Locate every blood parasite and identify its species.
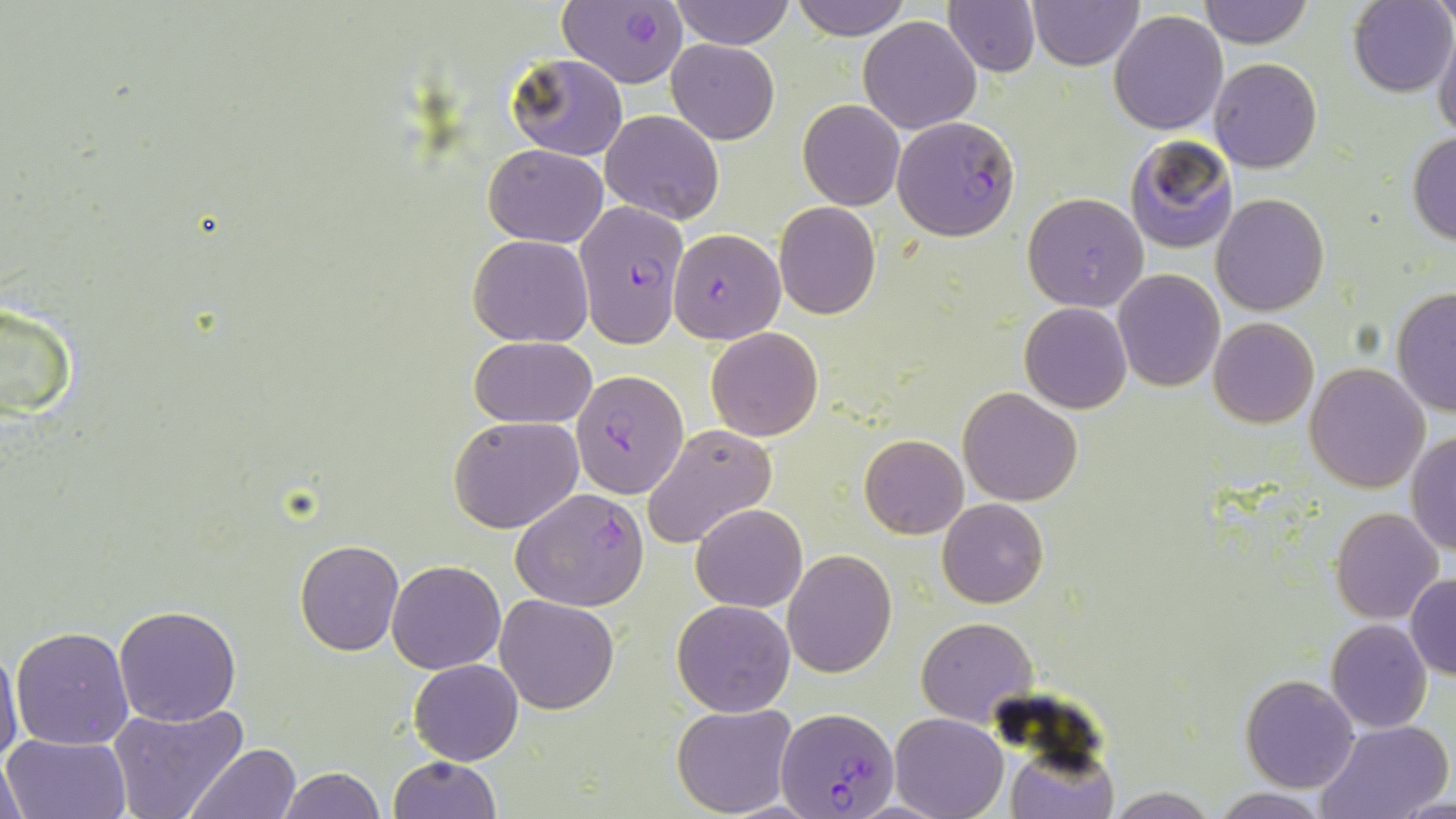

Approximate bounding boxes as (x1, y1, x2, y2) in pixels.
Plasmodium falciparum-infected red blood cells: (555, 1, 688, 89), (891, 116, 1020, 240), (573, 199, 690, 346), (668, 228, 785, 344), (572, 368, 690, 498), (511, 488, 649, 611), (777, 707, 898, 818).
No Plasmodium ovale, Plasmodium malariae, Plasmodium vivax, Babesia divergens, or Trypanosoma brucei observed.

Summary:
  - Uninfected red blood cell locations: (669, 0, 793, 49), (789, 0, 911, 40), (1199, 0, 1311, 47), (944, 1, 1040, 76), (1029, 1, 1141, 70), (1347, 1, 1454, 97), (1110, 9, 1227, 134), (1389, 12, 1452, 124), (859, 16, 981, 134), (1432, 25, 1456, 143), (666, 38, 779, 144), (505, 52, 627, 161), (1209, 57, 1322, 173), (798, 99, 904, 210), (601, 110, 725, 226), (1407, 132, 1456, 245), (1124, 135, 1238, 253), (484, 142, 608, 247), (1023, 192, 1149, 313), (1211, 193, 1329, 315), (774, 202, 881, 320), (468, 234, 593, 346), (1113, 269, 1225, 392), (1390, 285, 1456, 418), (1, 302, 78, 418), (1020, 302, 1131, 413), (1208, 317, 1318, 428), (706, 327, 823, 442), (470, 336, 597, 429), (1305, 364, 1431, 493), (958, 386, 1084, 505), (449, 417, 585, 534), (642, 424, 778, 548), (1407, 431, 1456, 556), (859, 433, 967, 539), (937, 498, 1049, 607), (692, 503, 806, 612), (1331, 508, 1443, 624), (295, 538, 405, 656), (783, 549, 897, 678), (387, 560, 505, 673), (1405, 574, 1456, 680), (495, 593, 620, 713), (673, 599, 795, 717), (113, 605, 241, 726), (915, 617, 1038, 726), (1325, 619, 1433, 734), (905, 621, 1022, 817), (10, 625, 134, 750), (0, 644, 24, 768), (410, 659, 523, 765), (1241, 674, 1360, 793), (108, 702, 248, 819), (672, 703, 798, 818), (890, 713, 1008, 819), (1313, 719, 1452, 819), (2, 734, 131, 819), (187, 743, 303, 818), (1009, 747, 1117, 819), (1, 748, 32, 817), (388, 756, 501, 818), (278, 767, 387, 819), (1208, 787, 1334, 819), (1394, 794, 1456, 818)
  - Slide-level diagnosis: Plasmodium falciparum
  - Magnification: 1000x
  - Preparation: thin blood smear
  - Image size: 1456×819 pixels
  - Modality: light microscopy
  - Field of view: single
  - Stain: May-Grünwald-Giemsa